Report the malaria status of this cell.
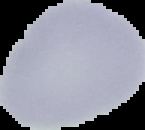

Uninfected.

Cell region segmented out of the field of view; the surrounding area is masked to black. Image is 145×130 pixels. From a thin blood smear.